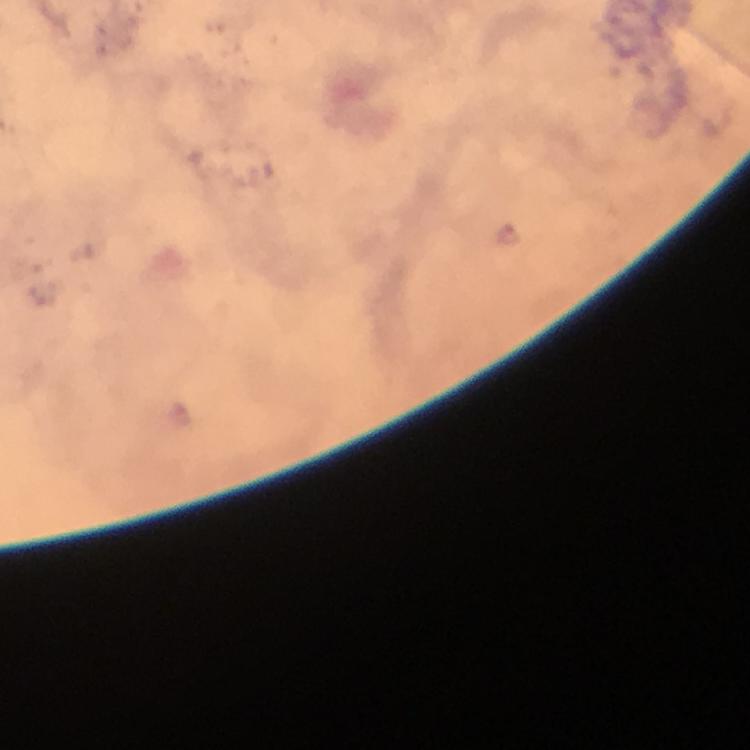
Approximate object centers, in pixels from the top-left corner.
Summary:
  - Plasmodium parasite locations: (x=509, y=234)
  - Magnification: 100x
  - Capture: smartphone camera through the microscope
  - Stain: Giemsa
  - Context: from a malaria diagnostic workup
  - Image size: 750×750 pixels
  - Cropped from: a single field of view
  - Immersion oil: applied
  - Preparation: thick blood film